Identify the blood parasite species.
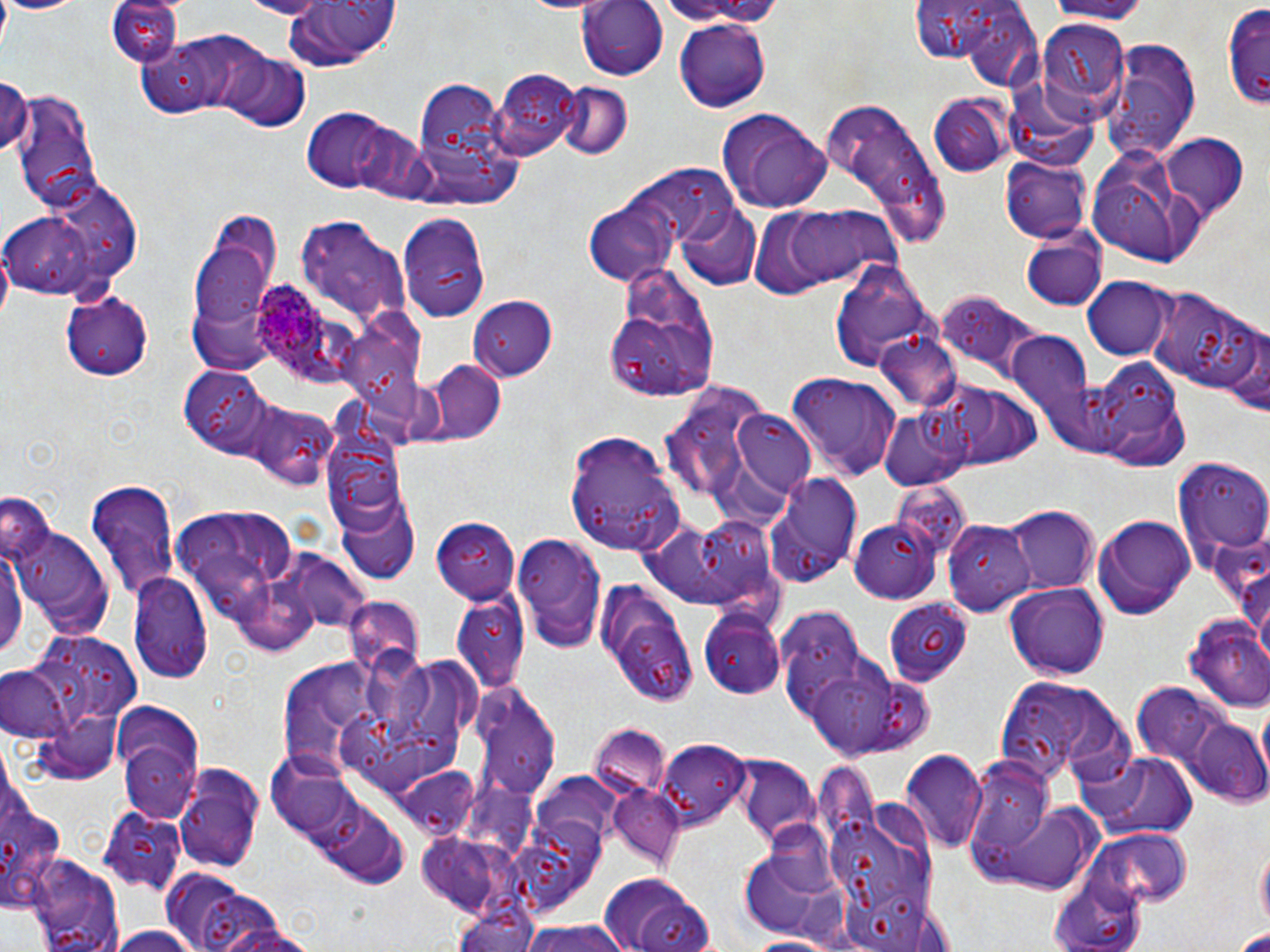
Plasmodium ovale.

Approximate bounding boxes as (x1, y1, x2, y2) in pixels. Plasmodium ovale-infected red blood cell locations: (250, 277, 324, 370). Uninfected red blood cell locations: (238, 0, 335, 18), (1038, 0, 1151, 22), (1, 1, 81, 16), (107, 1, 184, 68), (281, 1, 398, 75), (576, 1, 670, 79), (649, 1, 796, 26), (916, 2, 1046, 90), (1221, 4, 1270, 111), (674, 20, 771, 113), (1038, 20, 1132, 116), (142, 28, 269, 120), (1104, 37, 1202, 162), (217, 52, 311, 131), (490, 68, 580, 161), (0, 75, 35, 160), (408, 77, 520, 202), (557, 81, 632, 162), (10, 91, 102, 213), (930, 94, 1011, 177), (822, 100, 951, 249), (301, 108, 399, 192), (718, 111, 832, 214), (1160, 132, 1251, 220), (1085, 146, 1211, 266), (1001, 157, 1092, 242), (628, 164, 736, 252), (2, 187, 135, 302), (583, 201, 680, 284), (767, 204, 900, 293), (678, 205, 762, 290), (401, 213, 483, 285), (300, 217, 413, 329), (190, 222, 282, 364), (1018, 234, 1106, 311), (404, 249, 489, 315), (830, 259, 938, 372), (605, 266, 721, 399), (1083, 276, 1173, 360), (1149, 286, 1263, 396), (59, 290, 154, 381), (932, 291, 1050, 387), (468, 294, 558, 382), (1224, 327, 1269, 418), (335, 331, 437, 441), (1006, 332, 1100, 442), (874, 333, 963, 415), (1073, 356, 1190, 468), (416, 360, 505, 446), (181, 364, 276, 456), (788, 373, 902, 480), (654, 382, 782, 512), (938, 382, 1044, 470), (242, 398, 337, 489), (878, 406, 971, 489), (730, 412, 816, 500), (322, 417, 408, 540), (567, 431, 685, 556), (1171, 457, 1270, 567), (765, 470, 865, 587), (85, 477, 181, 603), (891, 479, 970, 556), (0, 493, 56, 567), (335, 493, 420, 588), (174, 505, 296, 599), (1009, 506, 1100, 594), (639, 514, 773, 613), (1092, 514, 1195, 619), (940, 515, 1032, 618), (433, 517, 524, 604), (848, 518, 938, 604), (851, 518, 939, 603), (8, 519, 116, 638), (941, 519, 1035, 615), (510, 531, 608, 653), (0, 535, 28, 663), (282, 550, 373, 635), (1234, 553, 1270, 666), (129, 573, 213, 686), (596, 580, 699, 705), (1007, 582, 1107, 679), (451, 593, 530, 695), (884, 593, 978, 687), (347, 596, 422, 680), (776, 606, 866, 714), (696, 608, 785, 699), (1183, 615, 1270, 715), (30, 630, 144, 724), (364, 645, 437, 748), (799, 655, 929, 761), (280, 656, 375, 780), (0, 665, 69, 744), (992, 676, 1133, 780), (468, 684, 560, 807), (1130, 684, 1229, 766), (113, 702, 207, 820), (1185, 719, 1270, 806), (589, 725, 671, 802), (658, 740, 748, 829), (1073, 747, 1201, 841), (900, 751, 987, 855), (269, 757, 356, 834), (738, 758, 817, 842), (811, 761, 886, 861), (389, 762, 479, 842), (175, 768, 263, 873), (0, 770, 66, 924), (532, 773, 623, 847), (607, 787, 685, 871), (970, 791, 1108, 894), (98, 808, 187, 894), (1082, 829, 1193, 913), (414, 837, 499, 908), (1257, 844, 1269, 933), (738, 846, 854, 945), (25, 848, 122, 952), (1049, 872, 1149, 951), (604, 873, 718, 952), (173, 879, 292, 952), (449, 902, 545, 952), (208, 921, 321, 952), (513, 921, 638, 951), (105, 926, 202, 952), (1232, 926, 1270, 950), (742, 933, 843, 952). Thin blood film. May-Grünwald-Giemsa-stained preparation. Single field of view. Image is 1270×952 pixels. 1000x magnification. Optical microscopy.